Report the malaria status of this cell.
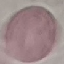

Uninfected.

Summary:
  - Capture: smartphone through the microscope eyepiece
  - Preparation: thin blood smear
  - Stain: Giemsa
  - Image type: cell patch, automatically extracted from a larger field of view and resized to 64 × 64 pixels